Point out each malaria parasite.
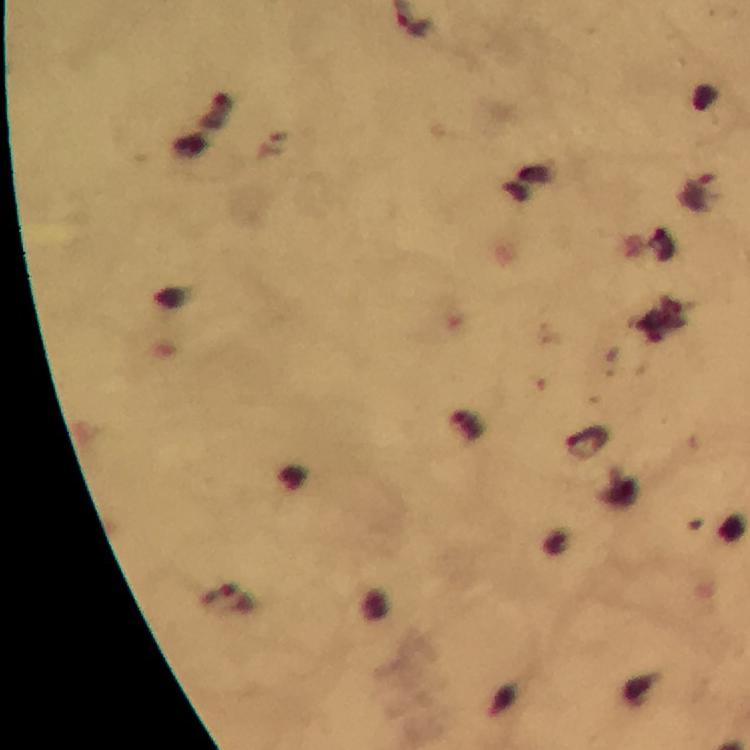

Approximate centers as [x, y] in pixels.
Malaria parasites: [701, 192], [584, 443], [227, 599].

context = from a diagnostic examination for malaria
capture = smartphone photograph through a microscope
image size = 750×750 pixels
immersion oil = applied
cropped from = one field of view
magnification = 100x
preparation = thick smear
stain = Giemsa